Assess this cell for malaria.
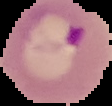

Parasitized.

Summary:
  - Image type: cell region segmented out of the field of view; surrounding area masked to black
  - Image size: 112×106 pixels
  - Preparation: thin blood smear